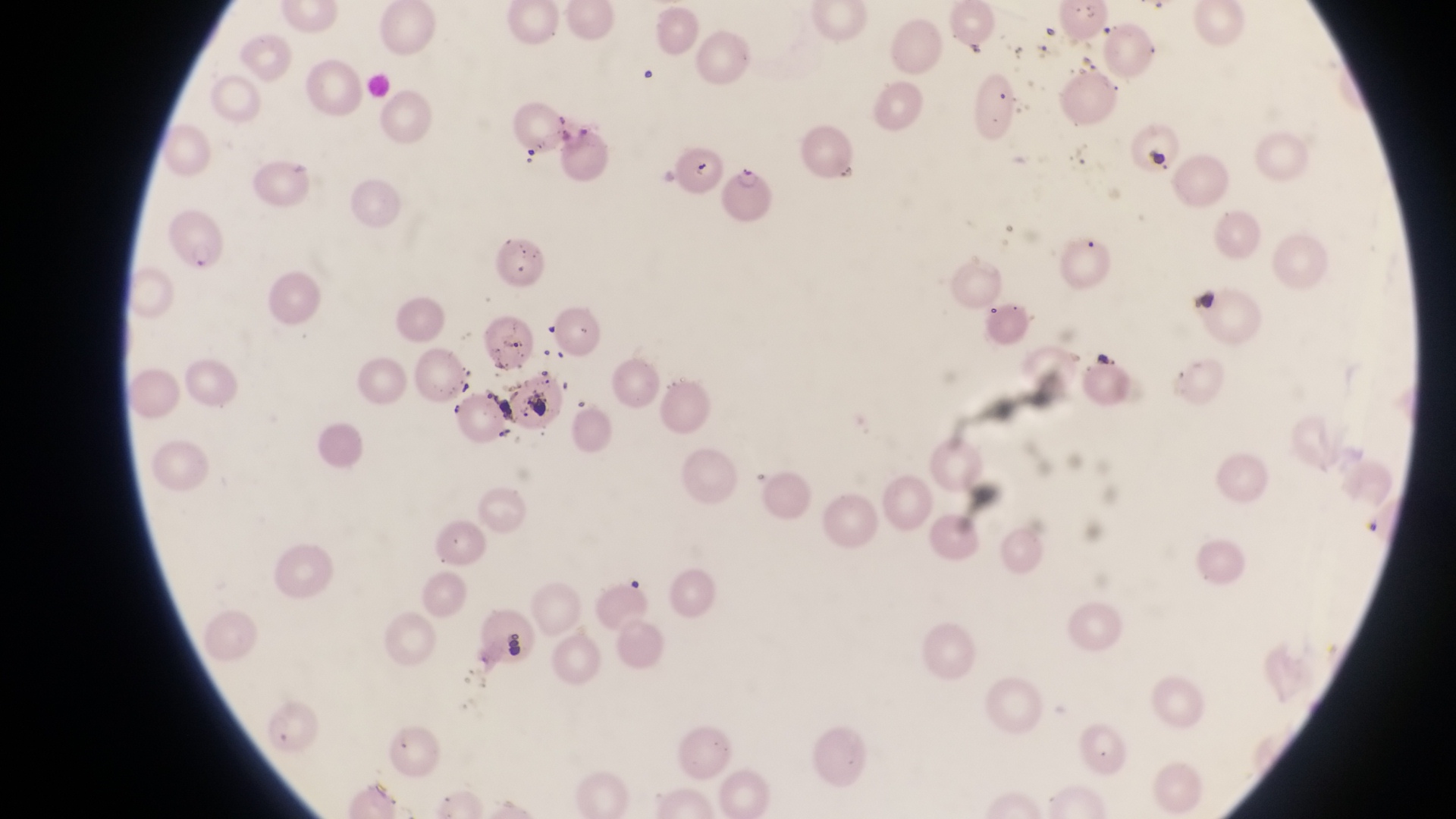

image size = 1456×819 pixels
magnification = 1000x
field of view = single
preparation = thin blood film
capture = smartphone photograph through the eyepiece of an Olympus CX-23 microscope
country = Uganda
parasitised red blood cell locations = approximate bounding boxes as left top right bottom in pixels: 732 166 777 219
artifact (platelet-like body, stain precipitate, or debris) locations = approximate bounding boxes as left top right bottom in pixels: 523 391 553 421; 504 626 531 660